Look for parasitized red blood cells.
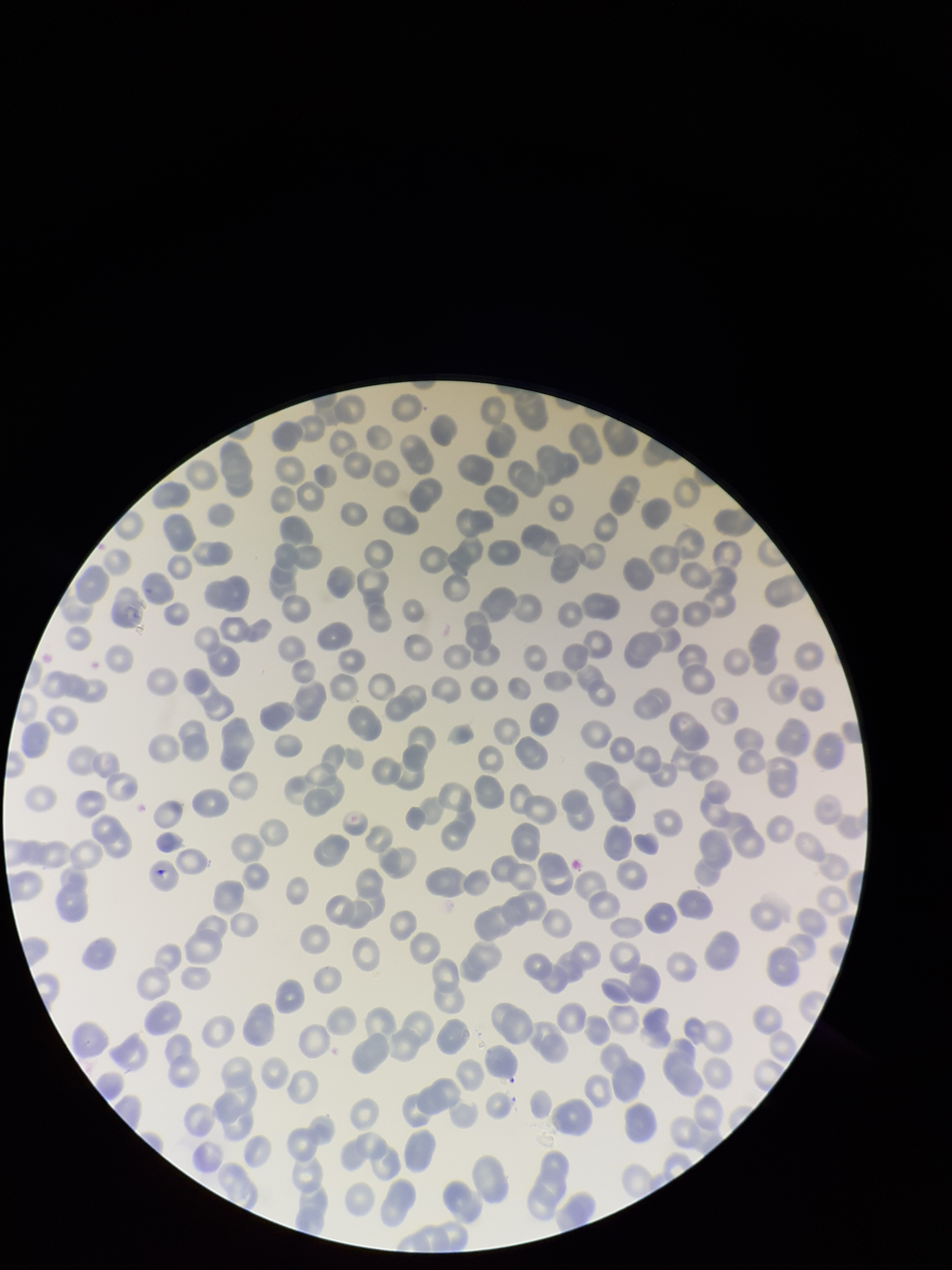
None identified.

species reported for this patient = Plasmodium falciparum
image size = 952×1270 pixels
field of view = one from this slide
patient malaria status = infected
capture = smartphone photograph through the microscope eyepiece
parasitized red blood cell count = 0
preparation = thin
stain = Giemsa
red blood cell count = 241